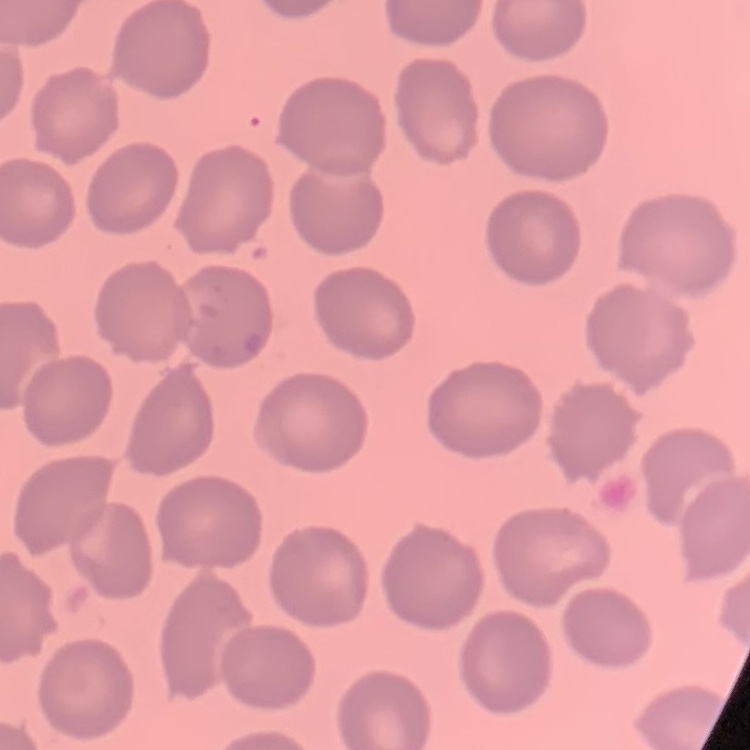

The erythrocytes show no rouleaux formation. Field's or Giemsa stain. One tile cut from a larger photomicrograph. Thin peripheral smear.